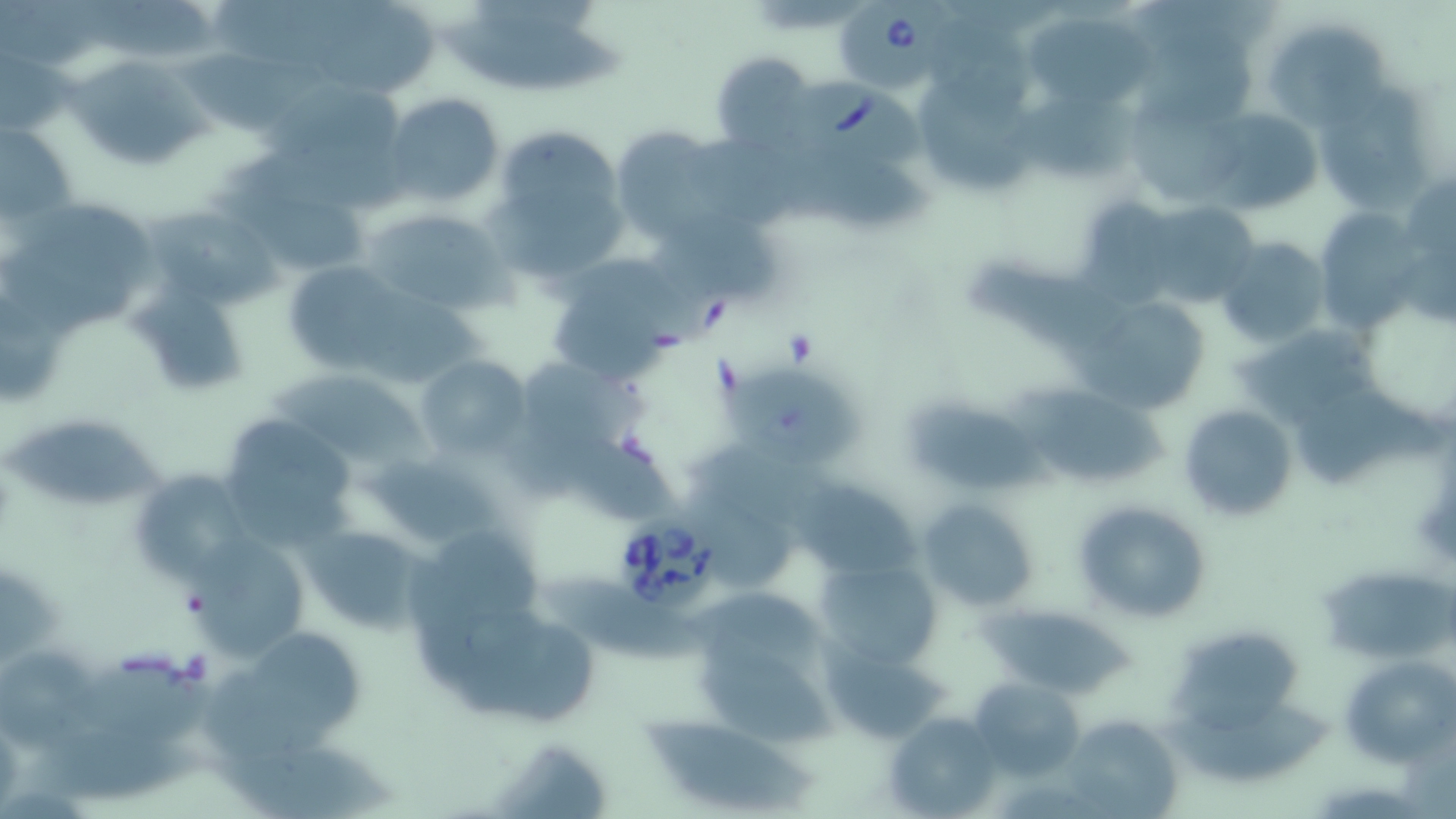

Summary:
  - Coordinate format: approximate bounding boxes as (x1,y1)-(x2,y2) corner pairs in pixels
  - Babesia divergens-infected red blood cell locations: (836,0)-(957,96), (793,71)-(929,167), (617,501)-(728,622)
  - Uninfected red blood cell locations: (203,2)-(368,67), (39,3)-(227,63), (319,5)-(437,97), (436,10)-(632,96), (1023,16)-(1157,113), (1140,26)-(1260,127), (1272,28)-(1388,137), (175,46)-(332,138), (1,49)-(72,138), (710,50)-(818,155), (60,61)-(226,171), (1319,75)-(1429,221), (923,86)-(1032,195), (252,88)-(408,175), (382,93)-(505,207), (1132,93)-(1253,204), (1004,102)-(1142,186), (1208,107)-(1319,213), (1,122)-(78,227), (489,126)-(631,280), (606,127)-(739,242), (208,190)-(369,277), (1073,193)-(1177,304), (15,200)-(164,301), (146,206)-(297,306), (360,207)-(507,315), (646,214)-(781,307), (1323,216)-(1422,332), (1212,235)-(1329,350), (281,259)-(411,375), (544,260)-(678,385), (973,261)-(1130,354), (134,282)-(247,396), (1072,291)-(1214,414), (1231,332)-(1385,429), (417,355)-(532,458), (723,370)-(862,470), (278,371)-(426,467), (1013,388)-(1173,487), (1302,389)-(1444,486), (911,402)-(1063,493), (1178,402)-(1298,521), (216,413)-(360,549), (1,421)-(173,508), (557,437)-(682,525), (365,448)-(501,550), (129,469)-(250,588), (795,476)-(922,582), (691,491)-(792,592), (918,498)-(1040,614), (1072,499)-(1213,624), (301,525)-(427,633), (184,533)-(311,659), (812,556)-(946,669), (1318,568)-(1456,662), (540,575)-(717,667), (983,603)-(1130,698), (462,623)-(595,730), (254,634)-(367,736), (820,635)-(952,745), (1168,635)-(1303,735), (700,640)-(837,744), (2,652)-(105,759), (1343,653)-(1454,767), (83,655)-(216,749), (202,668)-(331,761), (967,674)-(1087,778), (1153,695)-(1333,786), (882,711)-(1001,818), (640,715)-(813,811), (1061,716)-(1177,818), (16,732)-(213,809), (480,742)-(614,819), (203,743)-(407,819)
  - Slide-level diagnosis: Babesia divergens
  - Magnification: 1000x
  - Preparation: thin blood film
  - Modality: optical microscopy
  - Image size: 1456×819 pixels
  - Field of view: one of a larger specimen
  - Stain: May-Grünwald-Giemsa